Describe the morphology of the red blood cells.
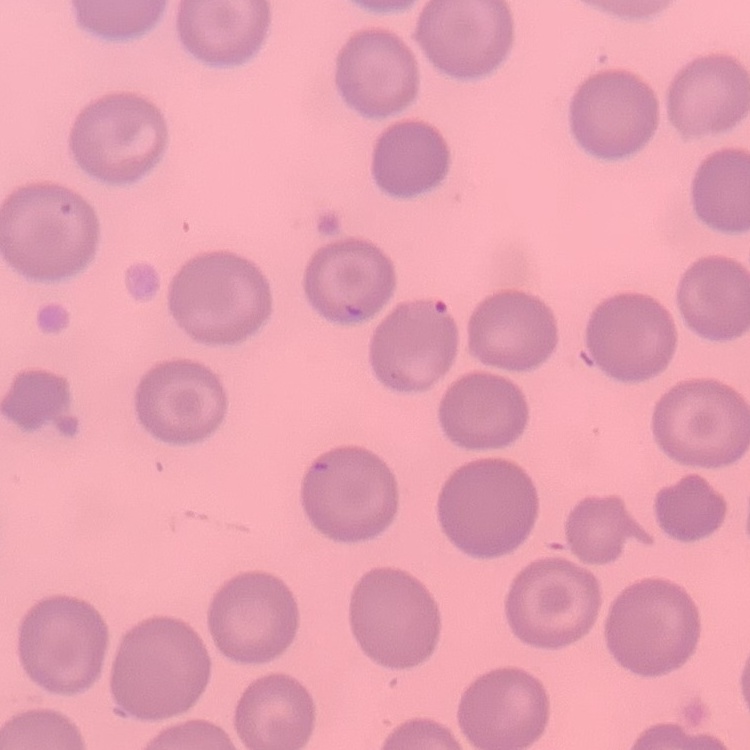
No rouleaux formation.

Field's or Giemsa stain. Square crop of a larger photomicrograph. Thin blood smear.